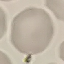 Malaria status: uninfected. Thin blood smear. Photographed with a smartphone camera at the microscope eyepiece. Giemsa-stained preparation. Cell patch, automatically extracted from a larger field of view and resized to 64 × 64 pixels.